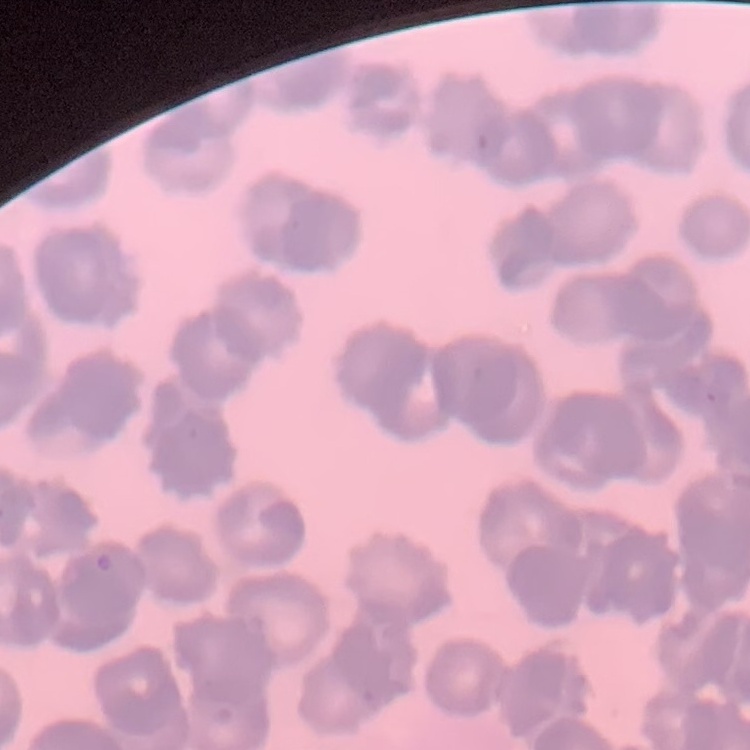 The erythrocytes show rouleaux formation. One tile cut from a larger photomicrograph. Thin peripheral smear. Field's or Giemsa stain.